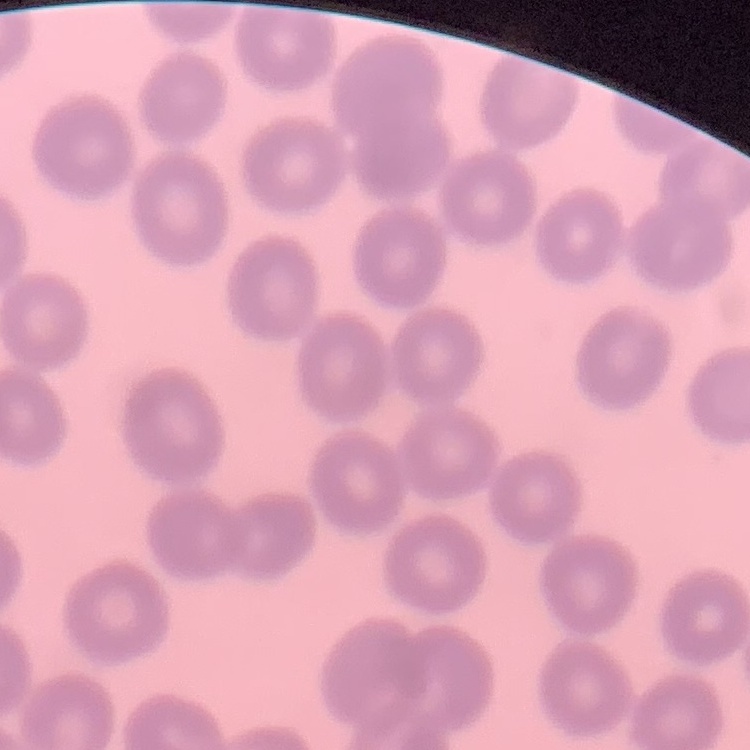

erythrocyte_morphology: no rouleaux formation
stain: Field's or Giemsa
image_type: one tile cut from a larger photomicrograph
preparation: thin peripheral smear